Classify this cell by malaria status.
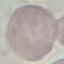

Uninfected.

Summary:
  - Preparation: thin blood film
  - Stain: Giemsa
  - Image type: automatically extracted cell patch, resized to 64 × 64 pixels
  - Capture: smartphone camera at the microscope eyepiece